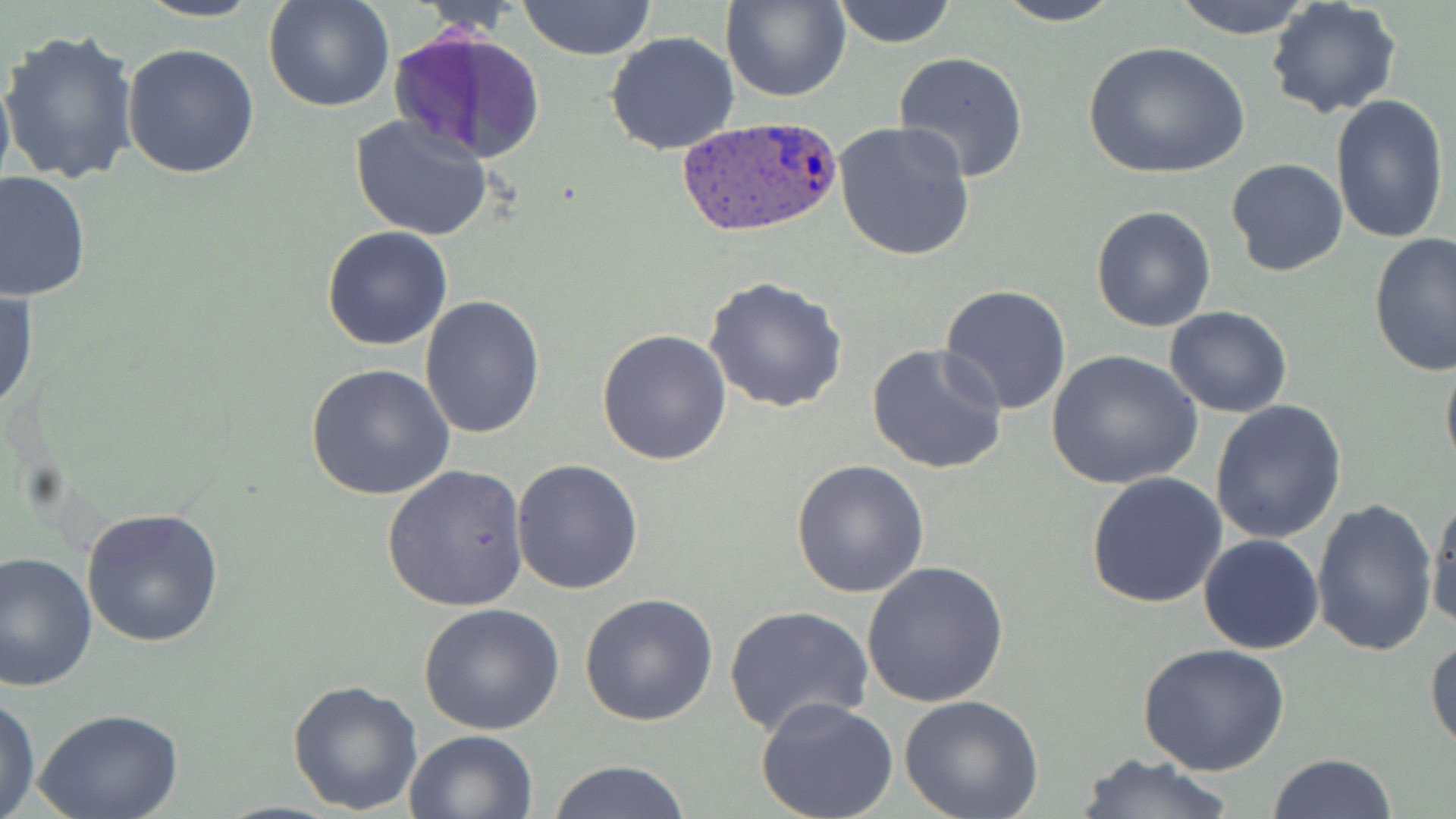 Approximate bounding boxes as [x1, y1, x2, y2] in pixels. Plasmodium ovale-infected red blood cell locations: [677, 116, 845, 238]. Uninfected red blood cell locations: [133, 0, 271, 22], [263, 0, 395, 113], [518, 0, 657, 61], [722, 0, 850, 102], [830, 0, 957, 48], [993, 0, 1123, 26], [1168, 0, 1318, 39], [1265, 1, 1403, 120], [2, 27, 140, 187], [389, 27, 547, 165], [606, 30, 740, 155], [1081, 40, 1250, 181], [120, 42, 261, 180], [893, 52, 1029, 182], [0, 61, 15, 203], [1329, 93, 1449, 245], [348, 114, 497, 243], [833, 118, 977, 261], [1226, 157, 1348, 278], [0, 171, 91, 301], [1091, 206, 1217, 332], [322, 224, 453, 351], [1368, 232, 1456, 380], [703, 275, 847, 414], [939, 284, 1073, 416], [1, 286, 37, 417], [419, 294, 546, 439], [1164, 306, 1293, 417], [596, 330, 733, 466], [1440, 341, 1456, 480], [866, 342, 1009, 474], [1044, 348, 1205, 491], [308, 363, 453, 503], [1210, 401, 1349, 545], [510, 458, 644, 595], [790, 459, 930, 599], [383, 465, 529, 612], [1086, 473, 1228, 610], [1426, 492, 1456, 631], [1311, 500, 1439, 657], [80, 509, 226, 649], [1197, 534, 1324, 656], [0, 552, 98, 692], [860, 561, 1009, 708], [578, 592, 718, 726], [417, 602, 565, 736], [724, 604, 875, 742], [1426, 636, 1456, 752], [1137, 643, 1291, 775], [287, 679, 423, 815], [0, 692, 40, 819], [899, 696, 1043, 819], [753, 697, 900, 819], [35, 709, 183, 819], [403, 729, 538, 818], [1267, 751, 1399, 819], [1077, 752, 1238, 819], [543, 759, 694, 819]. Slide-level diagnosis: Plasmodium ovale. Thin blood smear. Light microscopy. Image is 1456×819 pixels. Captured at 1000x magnification. Single field of view. May-Grünwald-Giemsa-stained preparation.